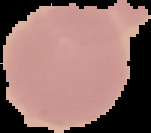

From a thin blood smear. The area outside the segmented cell region is set to black. Malaria status: uninfected. Image is 151×133 pixels.